Locate platelets.
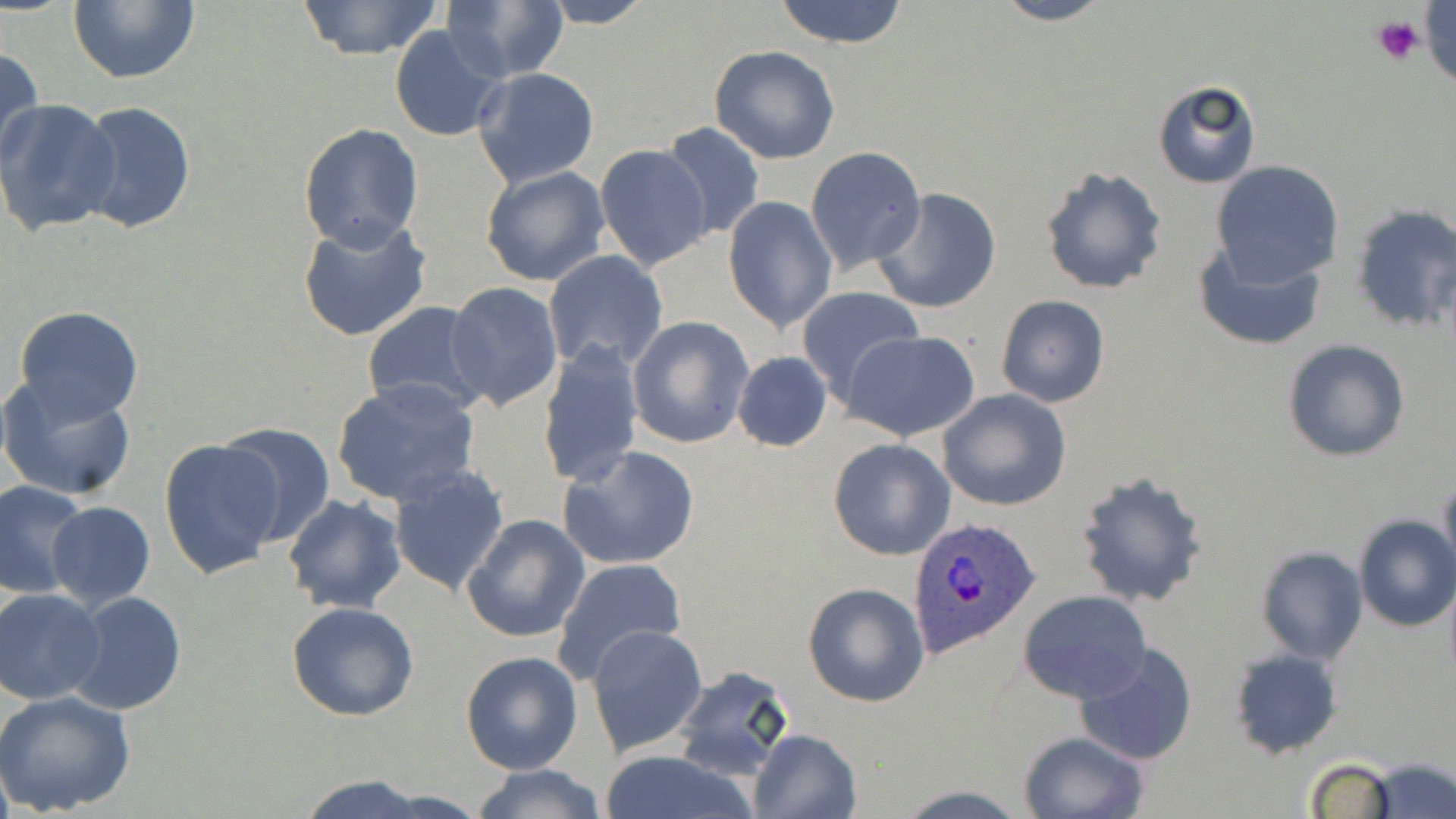
Approximate bounding boxes as (x1,y1)-(x2,y2) corner pairs in pixels.
Platelets: (1421,0)-(1456,85), (1372,15)-(1425,64).

{
  "slide_level_diagnosis": "Plasmodium ovale",
  "stain": "May-Grünwald-Giemsa",
  "modality": "light microscopy",
  "preparation": "thin blood smear",
  "uninfected_red_blood_cell_locations": "approximate bounding boxes as (x1,y1)-(x2,y2) corner pairs in pixels: (66,0)-(200,85), (296,0)-(444,59), (772,0)-(912,49), (987,0)-(1115,25), (443,1)-(566,85), (532,1)-(654,28), (389,24)-(504,144), (709,46)-(840,164), (0,48)-(45,171), (473,68)-(599,187), (1151,80)-(1261,188), (0,100)-(122,238), (72,100)-(196,234), (297,121)-(423,253), (659,121)-(765,241), (595,143)-(713,271), (805,146)-(927,272), (1211,160)-(1344,286), (480,164)-(611,286), (1039,164)-(1169,296), (871,187)-(1002,314), (723,196)-(836,334), (1349,200)-(1455,333), (296,216)-(432,343), (1192,239)-(1329,353), (544,250)-(668,374), (446,284)-(564,410), (797,287)-(926,405), (995,293)-(1109,407), (363,303)-(493,416), (12,306)-(145,425), (627,316)-(752,449), (845,328)-(980,441), (1282,339)-(1410,462), (538,341)-(646,489), (732,350)-(833,451), (0,374)-(139,500), (331,378)-(481,507), (937,388)-(1071,511), (217,423)-(335,544), (829,438)-(955,561), (159,439)-(285,581), (558,447)-(701,571), (387,462)-(509,596), (1074,470)-(1209,608), (1440,473)-(1456,578), (0,481)-(90,601), (283,494)-(407,614), (46,502)-(156,610), (461,513)-(589,644), (1353,515)-(1456,632), (1254,544)-(1369,664), (553,556)-(687,684), (803,581)-(929,705), (0,587)-(105,705), (1019,590)-(1152,706), (65,591)-(188,716), (286,601)-(418,721), (588,624)-(708,757), (1072,641)-(1201,768), (1228,648)-(1344,758), (460,650)-(582,775), (674,666)-(798,780), (0,690)-(136,816), (749,728)-(863,819), (1017,730)-(1148,819), (599,751)-(756,819), (1304,758)-(1395,819), (1368,759)-(1454,817), (466,763)-(607,819), (291,775)-(436,819), (890,785)-(1034,817)",
  "field_of_view": "single",
  "plasmodium_ovale_infected_red_blood_cell_locations": "approximate bounding boxes as (x1,y1)-(x2,y2) corner pairs in pixels: (907,517)-(1043,659)",
  "magnification": "1000x",
  "image_size": "1456×819 pixels"
}